State which parasite is depicted.
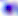
Toxoplasma gondii.

Summary:
  - Magnification: 400x
  - Modality: photomicrograph